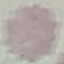
malaria status = uninfected
image type = automatically extracted cell patch, resized to 64 × 64 pixels
preparation = thin smear
capture = smartphone camera at the microscope eyepiece
stain = Giemsa